Name the cell type shown.
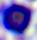

This is a leukocyte.

Photomicrograph. Captured at 400x magnification.